Name the parasite shown.
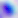

This is Toxoplasma gondii.

magnification = 400x
modality = photomicrograph